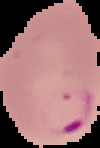
image size = 100×148 pixels
image type = cell region segmented out of the field of view; surrounding area masked to black
malaria status = parasitized
preparation = thin blood smear